Outline each blood parasite and name the species.
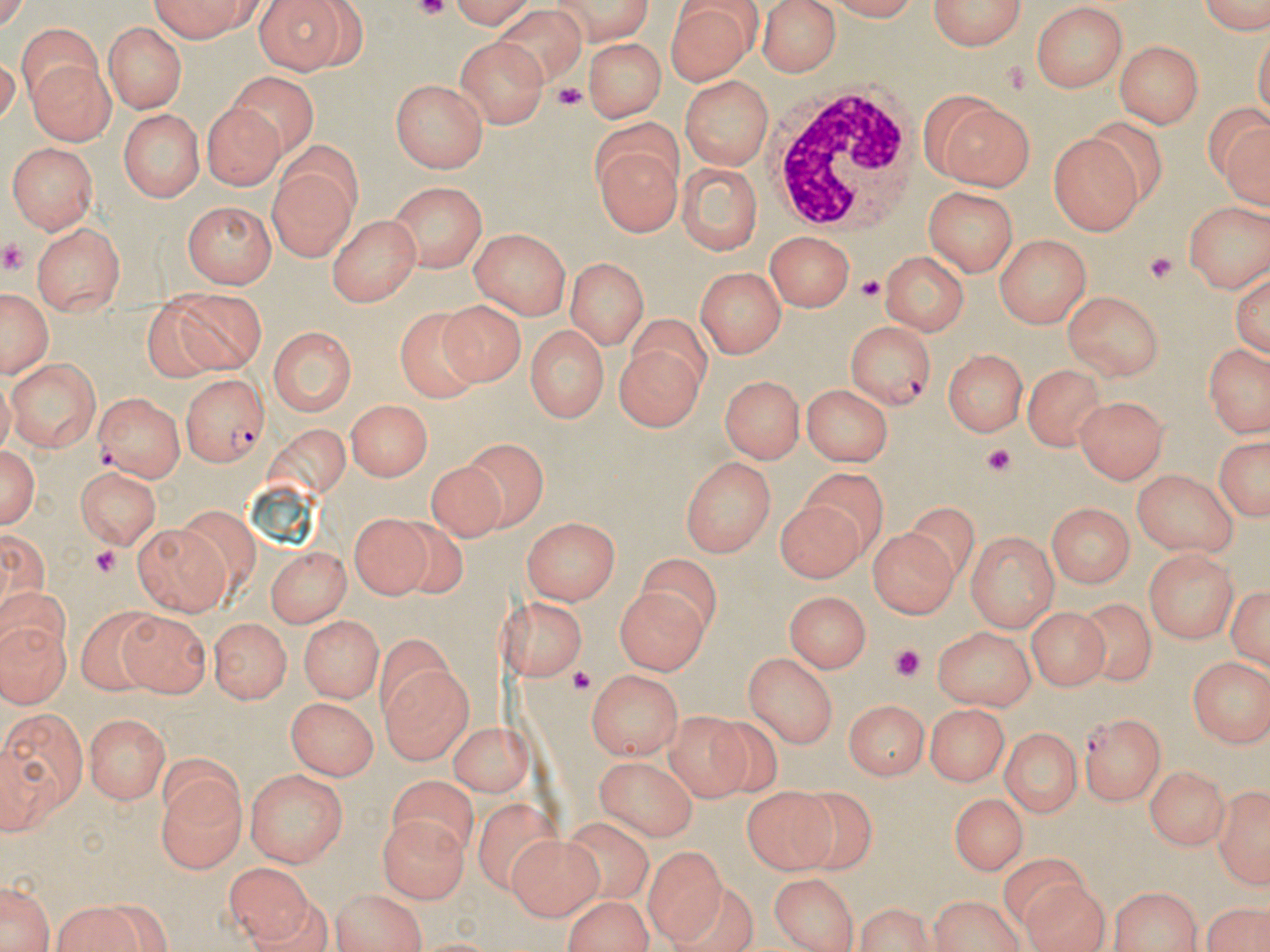
Approximate bounding boxes as named x1/y1/x2/y2 corners in pixels.
Plasmodium falciparum-infected red blood cells: (x1=846, y1=322, x2=934, y2=409), (x1=179, y1=373, x2=267, y2=468), (x1=1082, y1=712, x2=1166, y2=805).
No Plasmodium ovale, Plasmodium malariae, Plasmodium vivax, Babesia divergens, or Trypanosoma brucei observed.

slide_level_diagnosis: Plasmodium falciparum
magnification: 1000x
field_of_view: single
uninfected_red_blood_cell_locations: 'approximate bounding boxes as named x1/y1/x2/y2 corners in pixels: (x1=144, y1=0, x2=272, y2=38), (x1=254, y1=0, x2=364, y2=72), (x1=436, y1=0, x2=536, y2=27), (x1=540, y1=0, x2=658, y2=40), (x1=756, y1=0, x2=841, y2=77), (x1=925, y1=0, x2=1027, y2=52), (x1=1187, y1=0, x2=1270, y2=35), (x1=825, y1=1, x2=929, y2=23), (x1=669, y1=4, x2=758, y2=84), (x1=1032, y1=5, x2=1131, y2=95), (x1=492, y1=7, x2=584, y2=88), (x1=106, y1=21, x2=184, y2=110), (x1=13, y1=23, x2=99, y2=106), (x1=453, y1=34, x2=546, y2=125), (x1=580, y1=36, x2=669, y2=122), (x1=1116, y1=40, x2=1205, y2=129), (x1=21, y1=57, x2=110, y2=145), (x1=225, y1=72, x2=319, y2=150), (x1=680, y1=74, x2=774, y2=170), (x1=391, y1=79, x2=489, y2=173), (x1=928, y1=93, x2=1036, y2=189), (x1=198, y1=101, x2=286, y2=190), (x1=1204, y1=103, x2=1270, y2=212), (x1=120, y1=109, x2=206, y2=202), (x1=1049, y1=132, x2=1141, y2=232), (x1=7, y1=141, x2=100, y2=232), (x1=593, y1=141, x2=676, y2=237), (x1=266, y1=156, x2=360, y2=262), (x1=676, y1=161, x2=761, y2=253), (x1=389, y1=183, x2=487, y2=271), (x1=922, y1=188, x2=1018, y2=277), (x1=1184, y1=198, x2=1270, y2=291), (x1=181, y1=199, x2=275, y2=287), (x1=327, y1=212, x2=420, y2=306), (x1=35, y1=223, x2=124, y2=315), (x1=467, y1=228, x2=572, y2=318), (x1=767, y1=232, x2=856, y2=314), (x1=993, y1=233, x2=1090, y2=326), (x1=878, y1=251, x2=970, y2=335), (x1=565, y1=259, x2=646, y2=348), (x1=1232, y1=262, x2=1270, y2=359), (x1=695, y1=266, x2=784, y2=358), (x1=0, y1=286, x2=54, y2=380), (x1=139, y1=288, x2=217, y2=383), (x1=170, y1=290, x2=264, y2=373), (x1=1063, y1=290, x2=1165, y2=381), (x1=441, y1=300, x2=526, y2=387), (x1=394, y1=307, x2=478, y2=401), (x1=629, y1=314, x2=716, y2=392), (x1=525, y1=322, x2=609, y2=423), (x1=267, y1=324, x2=356, y2=417), (x1=616, y1=336, x2=705, y2=432), (x1=1204, y1=344, x2=1267, y2=439), (x1=944, y1=349, x2=1028, y2=436), (x1=7, y1=357, x2=100, y2=452), (x1=1028, y1=363, x2=1106, y2=447), (x1=721, y1=374, x2=804, y2=460), (x1=802, y1=382, x2=892, y2=466), (x1=94, y1=391, x2=182, y2=482), (x1=1076, y1=396, x2=1166, y2=485), (x1=345, y1=398, x2=433, y2=484), (x1=1210, y1=434, x2=1270, y2=523), (x1=468, y1=441, x2=550, y2=534), (x1=1, y1=442, x2=40, y2=530), (x1=424, y1=453, x2=512, y2=533), (x1=679, y1=454, x2=779, y2=555), (x1=76, y1=461, x2=162, y2=548), (x1=799, y1=466, x2=886, y2=552), (x1=1132, y1=469, x2=1236, y2=557), (x1=774, y1=499, x2=863, y2=583), (x1=908, y1=502, x2=976, y2=588), (x1=1049, y1=502, x2=1132, y2=591), (x1=347, y1=513, x2=427, y2=601), (x1=397, y1=516, x2=468, y2=607), (x1=524, y1=517, x2=621, y2=604), (x1=132, y1=523, x2=229, y2=614), (x1=870, y1=526, x2=957, y2=619), (x1=968, y1=529, x2=1057, y2=633), (x1=263, y1=546, x2=353, y2=622), (x1=1141, y1=549, x2=1236, y2=647), (x1=640, y1=554, x2=722, y2=640), (x1=1229, y1=579, x2=1270, y2=675), (x1=615, y1=585, x2=709, y2=675), (x1=785, y1=590, x2=871, y2=674), (x1=505, y1=595, x2=588, y2=685), (x1=1079, y1=600, x2=1155, y2=686), (x1=1028, y1=604, x2=1109, y2=692), (x1=0, y1=605, x2=68, y2=710), (x1=75, y1=610, x2=163, y2=693), (x1=120, y1=612, x2=210, y2=696), (x1=298, y1=614, x2=382, y2=703), (x1=208, y1=619, x2=292, y2=704), (x1=934, y1=626, x2=1035, y2=710), (x1=744, y1=652, x2=834, y2=748), (x1=1186, y1=655, x2=1267, y2=749), (x1=382, y1=665, x2=472, y2=761), (x1=586, y1=671, x2=683, y2=761), (x1=844, y1=698, x2=927, y2=781), (x1=287, y1=699, x2=376, y2=779), (x1=927, y1=704, x2=1008, y2=787), (x1=666, y1=707, x2=750, y2=800), (x1=1, y1=709, x2=87, y2=826), (x1=83, y1=713, x2=173, y2=804), (x1=448, y1=720, x2=530, y2=796), (x1=705, y1=720, x2=783, y2=798), (x1=1000, y1=726, x2=1082, y2=819), (x1=594, y1=756, x2=695, y2=840), (x1=1147, y1=766, x2=1228, y2=853), (x1=244, y1=768, x2=345, y2=867), (x1=155, y1=770, x2=245, y2=874), (x1=386, y1=774, x2=476, y2=860), (x1=1211, y1=778, x2=1270, y2=888), (x1=742, y1=789, x2=832, y2=873), (x1=947, y1=791, x2=1027, y2=873), (x1=788, y1=793, x2=876, y2=868), (x1=473, y1=799, x2=564, y2=899), (x1=567, y1=816, x2=655, y2=906), (x1=381, y1=817, x2=470, y2=903), (x1=509, y1=837, x2=602, y2=921), (x1=642, y1=849, x2=727, y2=945), (x1=999, y1=852, x2=1088, y2=921), (x1=225, y1=865, x2=315, y2=946), (x1=770, y1=873, x2=858, y2=950), (x1=1, y1=877, x2=55, y2=952), (x1=1021, y1=880, x2=1109, y2=952), (x1=670, y1=886, x2=753, y2=952), (x1=1107, y1=886, x2=1202, y2=952), (x1=328, y1=890, x2=427, y2=952), (x1=927, y1=894, x2=1028, y2=952), (x1=557, y1=895, x2=659, y2=951), (x1=50, y1=898, x2=151, y2=951), (x1=1205, y1=898, x2=1269, y2=952), (x1=849, y1=899, x2=937, y2=952)'
image_size: 1270×952 pixels
white_blood_cell_locations: 'approximate bounding boxes as named x1/y1/x2/y2 corners in pixels: (x1=767, y1=83, x2=918, y2=231)'
modality: optical microscopy
stain: May-Grünwald-Giemsa
preparation: thin blood film
platelet_locations: 'approximate bounding boxes as named x1/y1/x2/y2 corners in pixels: (x1=414, y1=2, x2=456, y2=20), (x1=997, y1=58, x2=1030, y2=96), (x1=554, y1=84, x2=584, y2=107), (x1=0, y1=238, x2=27, y2=275), (x1=1142, y1=251, x2=1174, y2=285), (x1=855, y1=273, x2=884, y2=302), (x1=981, y1=445, x2=1014, y2=475), (x1=87, y1=545, x2=123, y2=577), (x1=891, y1=647, x2=922, y2=680), (x1=563, y1=663, x2=595, y2=694)'